Find each WBC.
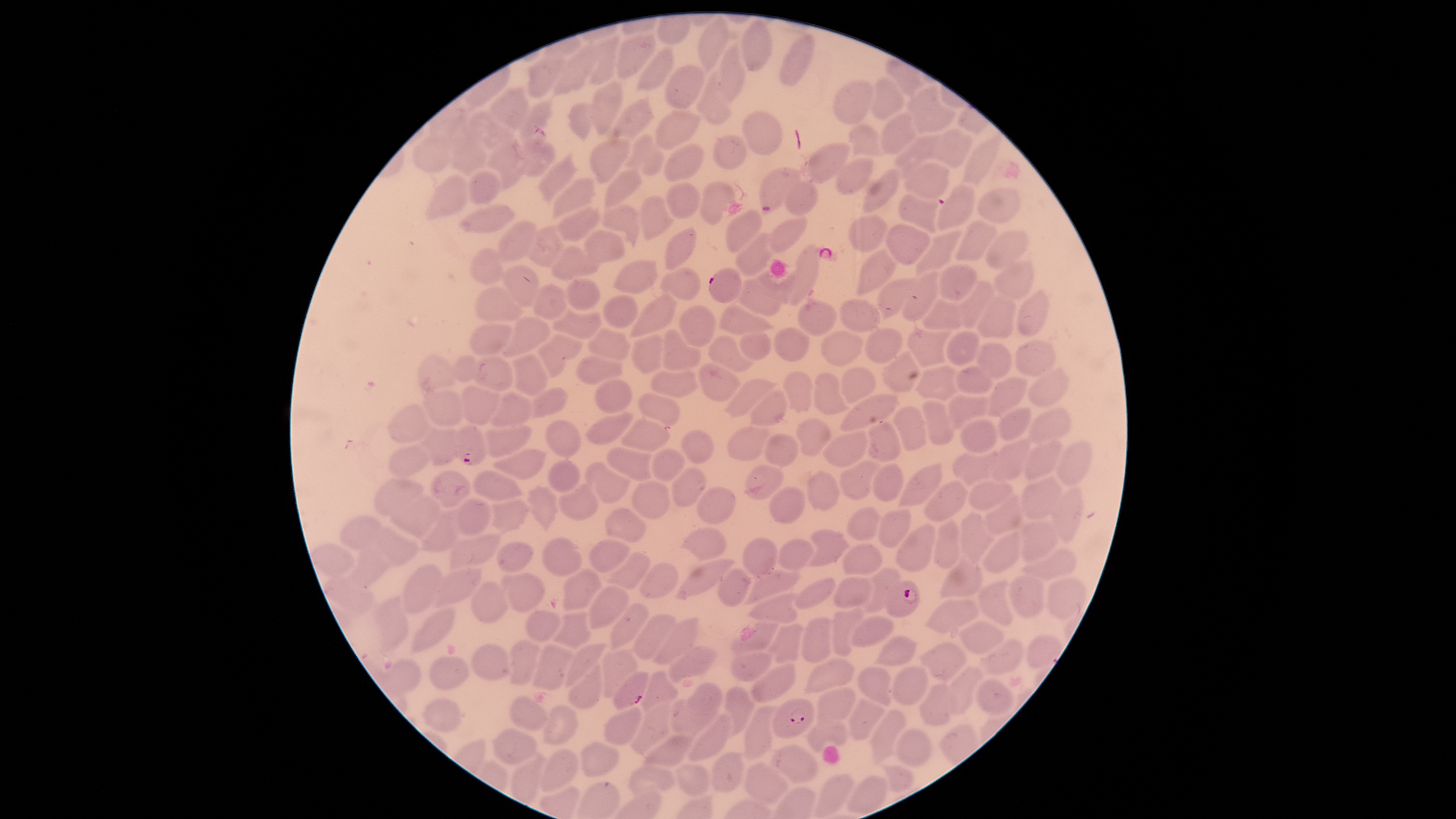
No WBCs identified.

Approximate bounding boxes, in pixels from the top-left corner.
Summary:
  - Parasitized RBCs: (left=520, top=124, right=555, bottom=177), (left=709, top=268, right=742, bottom=303), (left=453, top=425, right=489, bottom=466), (left=884, top=580, right=921, bottom=617), (left=611, top=672, right=650, bottom=710), (left=771, top=698, right=814, bottom=739)
  - Uninfected RBCs: (left=698, top=15, right=730, bottom=75), (left=740, top=19, right=772, bottom=75), (left=615, top=31, right=657, bottom=80), (left=778, top=32, right=815, bottom=86), (left=588, top=35, right=620, bottom=86), (left=717, top=37, right=747, bottom=105), (left=551, top=41, right=596, bottom=97), (left=636, top=46, right=674, bottom=93), (left=525, top=51, right=568, bottom=100), (left=664, top=64, right=707, bottom=109), (left=695, top=69, right=734, bottom=125), (left=871, top=77, right=904, bottom=120), (left=592, top=80, right=623, bottom=136), (left=833, top=80, right=874, bottom=125), (left=906, top=84, right=957, bottom=133), (left=489, top=86, right=529, bottom=130), (left=611, top=92, right=656, bottom=141), (left=517, top=98, right=553, bottom=142), (left=567, top=102, right=596, bottom=142), (left=465, top=108, right=509, bottom=151), (left=741, top=109, right=783, bottom=157), (left=655, top=110, right=702, bottom=151), (left=878, top=113, right=918, bottom=155), (left=847, top=123, right=884, bottom=161), (left=928, top=130, right=972, bottom=169), (left=450, top=132, right=488, bottom=179), (left=961, top=132, right=1002, bottom=186), (left=485, top=133, right=526, bottom=193), (left=620, top=133, right=665, bottom=177), (left=894, top=133, right=942, bottom=176), (left=711, top=134, right=749, bottom=172), (left=411, top=135, right=453, bottom=174), (left=589, top=138, right=631, bottom=185), (left=663, top=142, right=704, bottom=183), (left=806, top=142, right=851, bottom=184), (left=537, top=149, right=579, bottom=204), (left=833, top=155, right=874, bottom=195), (left=904, top=162, right=951, bottom=201), (left=759, top=166, right=805, bottom=216), (left=604, top=167, right=644, bottom=207), (left=862, top=168, right=900, bottom=213), (left=466, top=169, right=501, bottom=204), (left=424, top=173, right=470, bottom=220), (left=551, top=176, right=597, bottom=220), (left=784, top=178, right=819, bottom=216), (left=699, top=180, right=736, bottom=226), (left=665, top=181, right=700, bottom=219), (left=935, top=183, right=975, bottom=230), (left=977, top=187, right=1020, bottom=224), (left=897, top=193, right=939, bottom=234), (left=639, top=194, right=675, bottom=241), (left=456, top=201, right=517, bottom=236), (left=600, top=204, right=642, bottom=248), (left=558, top=205, right=601, bottom=243), (left=725, top=208, right=763, bottom=254), (left=848, top=214, right=888, bottom=252), (left=770, top=216, right=808, bottom=252), (left=955, top=218, right=999, bottom=261), (left=494, top=219, right=537, bottom=265), (left=886, top=224, right=931, bottom=265), (left=526, top=225, right=566, bottom=267), (left=664, top=226, right=697, bottom=271), (left=581, top=229, right=626, bottom=265), (left=914, top=229, right=962, bottom=277), (left=985, top=230, right=1030, bottom=270), (left=733, top=231, right=777, bottom=277), (left=787, top=242, right=821, bottom=308), (left=550, top=246, right=600, bottom=281), (left=470, top=247, right=504, bottom=286), (left=855, top=248, right=898, bottom=297), (left=992, top=257, right=1034, bottom=298), (left=612, top=259, right=659, bottom=295), (left=501, top=263, right=540, bottom=307), (left=938, top=263, right=978, bottom=302), (left=660, top=267, right=701, bottom=302), (left=730, top=269, right=793, bottom=317), (left=901, top=270, right=939, bottom=321), (left=565, top=277, right=601, bottom=312), (left=877, top=277, right=917, bottom=320), (left=955, top=279, right=994, bottom=329), (left=531, top=283, right=569, bottom=320), (left=474, top=286, right=524, bottom=323), (left=1016, top=287, right=1049, bottom=336), (left=601, top=294, right=639, bottom=330), (left=628, top=294, right=678, bottom=338), (left=975, top=294, right=1017, bottom=340), (left=922, top=296, right=961, bottom=332), (left=797, top=298, right=838, bottom=337), (left=839, top=298, right=881, bottom=333), (left=679, top=304, right=716, bottom=347), (left=717, top=304, right=775, bottom=335), (left=552, top=305, right=601, bottom=339), (left=501, top=316, right=551, bottom=359), (left=469, top=323, right=514, bottom=357), (left=906, top=326, right=953, bottom=368), (left=586, top=327, right=632, bottom=361), (left=773, top=327, right=810, bottom=362), (left=661, top=328, right=703, bottom=372), (left=864, top=328, right=904, bottom=364), (left=820, top=329, right=865, bottom=367), (left=945, top=329, right=981, bottom=367), (left=738, top=332, right=772, bottom=360), (left=536, top=333, right=585, bottom=382), (left=631, top=334, right=665, bottom=373), (left=707, top=335, right=756, bottom=373), (left=1015, top=339, right=1057, bottom=377), (left=976, top=342, right=1013, bottom=378), (left=882, top=349, right=921, bottom=392), (left=510, top=353, right=550, bottom=398), (left=418, top=354, right=455, bottom=392), (left=470, top=354, right=514, bottom=391), (left=452, top=355, right=479, bottom=384), (left=574, top=355, right=623, bottom=385), (left=697, top=360, right=742, bottom=401), (left=914, top=363, right=961, bottom=402), (left=954, top=365, right=991, bottom=395), (left=1025, top=365, right=1071, bottom=408), (left=840, top=367, right=876, bottom=403), (left=650, top=370, right=700, bottom=399), (left=782, top=370, right=814, bottom=414), (left=812, top=371, right=853, bottom=415), (left=721, top=377, right=782, bottom=418), (left=986, top=377, right=1029, bottom=417), (left=594, top=379, right=633, bottom=415), (left=460, top=385, right=502, bottom=425), (left=530, top=386, right=568, bottom=418), (left=422, top=388, right=464, bottom=428), (left=490, top=389, right=533, bottom=427), (left=749, top=389, right=790, bottom=427), (left=638, top=392, right=681, bottom=427), (left=840, top=392, right=898, bottom=431), (left=945, top=392, right=990, bottom=430), (left=922, top=398, right=955, bottom=445), (left=387, top=404, right=432, bottom=443), (left=893, top=405, right=928, bottom=453), (left=998, top=406, right=1032, bottom=442), (left=1028, top=406, right=1072, bottom=443), (left=585, top=410, right=633, bottom=445), (left=620, top=416, right=671, bottom=453), (left=545, top=417, right=583, bottom=458), (left=794, top=418, right=831, bottom=457), (left=960, top=418, right=998, bottom=454), (left=867, top=421, right=901, bottom=464), (left=484, top=424, right=533, bottom=459), (left=420, top=425, right=458, bottom=467), (left=726, top=425, right=771, bottom=462), (left=680, top=429, right=715, bottom=465), (left=822, top=429, right=869, bottom=468), (left=762, top=433, right=799, bottom=468), (left=991, top=436, right=1031, bottom=482), (left=1024, top=437, right=1064, bottom=480), (left=1056, top=439, right=1093, bottom=486), (left=387, top=443, right=430, bottom=481), (left=606, top=446, right=657, bottom=482), (left=491, top=447, right=547, bottom=480), (left=651, top=448, right=686, bottom=482), (left=951, top=449, right=999, bottom=486), (left=838, top=457, right=884, bottom=501), (left=546, top=458, right=581, bottom=493), (left=584, top=461, right=634, bottom=504), (left=897, top=461, right=943, bottom=507), (left=744, top=462, right=784, bottom=500), (left=871, top=462, right=902, bottom=501), (left=672, top=465, right=707, bottom=506), (left=429, top=469, right=473, bottom=510), (left=472, top=469, right=525, bottom=501), (left=806, top=469, right=841, bottom=511), (left=1021, top=474, right=1064, bottom=520), (left=373, top=476, right=424, bottom=516), (left=923, top=479, right=971, bottom=523), (left=968, top=479, right=1013, bottom=511), (left=631, top=480, right=671, bottom=520), (left=558, top=482, right=599, bottom=521), (left=526, top=484, right=560, bottom=534), (left=769, top=484, right=806, bottom=526), (left=1051, top=486, right=1084, bottom=545), (left=694, top=487, right=736, bottom=525), (left=981, top=493, right=1025, bottom=535), (left=389, top=496, right=441, bottom=539), (left=454, top=497, right=491, bottom=537), (left=490, top=498, right=531, bottom=534), (left=845, top=506, right=882, bottom=542), (left=604, top=507, right=648, bottom=544), (left=877, top=507, right=913, bottom=549), (left=417, top=509, right=460, bottom=551), (left=958, top=510, right=995, bottom=568), (left=338, top=515, right=383, bottom=551), (left=931, top=520, right=961, bottom=571), (left=1019, top=521, right=1057, bottom=562), (left=895, top=522, right=936, bottom=573), (left=372, top=526, right=420, bottom=567), (left=680, top=526, right=728, bottom=562), (left=805, top=528, right=851, bottom=568), (left=981, top=528, right=1021, bottom=573), (left=448, top=533, right=501, bottom=570), (left=541, top=535, right=583, bottom=577), (left=742, top=537, right=779, bottom=578), (left=778, top=537, right=815, bottom=569), (left=588, top=538, right=631, bottom=574), (left=496, top=540, right=533, bottom=575), (left=842, top=543, right=884, bottom=577), (left=349, top=547, right=389, bottom=586), (left=1022, top=547, right=1077, bottom=581), (left=605, top=551, right=651, bottom=589), (left=675, top=558, right=737, bottom=600), (left=939, top=558, right=984, bottom=599), (left=640, top=562, right=680, bottom=598), (left=402, top=563, right=443, bottom=616), (left=430, top=566, right=483, bottom=609), (left=716, top=566, right=754, bottom=608), (left=864, top=566, right=901, bottom=614), (left=563, top=567, right=603, bottom=612), (left=745, top=568, right=801, bottom=604), (left=500, top=571, right=545, bottom=613), (left=322, top=575, right=375, bottom=616), (left=833, top=576, right=875, bottom=609), (left=1007, top=576, right=1046, bottom=619), (left=793, top=577, right=837, bottom=609), (left=1046, top=577, right=1090, bottom=619), (left=977, top=579, right=1014, bottom=627), (left=471, top=580, right=509, bottom=623), (left=588, top=585, right=631, bottom=630), (left=748, top=589, right=799, bottom=624), (left=370, top=594, right=410, bottom=652), (left=925, top=599, right=980, bottom=633), (left=609, top=604, right=651, bottom=651), (left=410, top=606, right=457, bottom=655), (left=523, top=608, right=562, bottom=643), (left=830, top=609, right=866, bottom=656), (left=552, top=610, right=592, bottom=649), (left=632, top=612, right=677, bottom=660), (left=851, top=615, right=895, bottom=647), (left=801, top=616, right=836, bottom=665), (left=651, top=617, right=699, bottom=664), (left=728, top=620, right=782, bottom=656), (left=958, top=621, right=1005, bottom=655), (left=766, top=622, right=804, bottom=664), (left=873, top=634, right=921, bottom=668), (left=1025, top=634, right=1063, bottom=670), (left=507, top=638, right=541, bottom=686), (left=981, top=639, right=1025, bottom=676), (left=918, top=641, right=969, bottom=684), (left=471, top=642, right=509, bottom=681), (left=563, top=642, right=608, bottom=689), (left=529, top=644, right=574, bottom=690), (left=668, top=644, right=718, bottom=683), (left=600, top=648, right=641, bottom=697), (left=729, top=650, right=773, bottom=683), (left=428, top=654, right=470, bottom=691), (left=804, top=657, right=856, bottom=695), (left=386, top=659, right=421, bottom=695), (left=566, top=659, right=601, bottom=710), (left=750, top=663, right=797, bottom=704), (left=947, top=664, right=986, bottom=716), (left=891, top=665, right=930, bottom=706), (left=857, top=666, right=892, bottom=706), (left=641, top=669, right=679, bottom=714), (left=974, top=678, right=1015, bottom=715), (left=685, top=682, right=723, bottom=714), (left=917, top=683, right=959, bottom=727), (left=723, top=685, right=757, bottom=738), (left=817, top=685, right=857, bottom=721), (left=508, top=694, right=549, bottom=732), (left=421, top=697, right=462, bottom=733), (left=847, top=698, right=888, bottom=742), (left=669, top=699, right=719, bottom=739), (left=629, top=700, right=671, bottom=755), (left=540, top=703, right=580, bottom=744), (left=742, top=704, right=782, bottom=761), (left=604, top=706, right=643, bottom=746), (left=868, top=709, right=907, bottom=769), (left=686, top=713, right=731, bottom=762), (left=806, top=718, right=849, bottom=753), (left=488, top=727, right=539, bottom=763), (left=896, top=727, right=933, bottom=767), (left=641, top=733, right=694, bottom=769), (left=580, top=740, right=620, bottom=778), (left=770, top=743, right=817, bottom=784), (left=540, top=748, right=580, bottom=791), (left=509, top=750, right=547, bottom=805), (left=711, top=750, right=745, bottom=793), (left=743, top=761, right=789, bottom=805), (left=675, top=762, right=710, bottom=797), (left=879, top=762, right=915, bottom=792), (left=628, top=763, right=675, bottom=796), (left=814, top=773, right=854, bottom=818), (left=846, top=774, right=888, bottom=815)
  - Stain: Giemsa
  - Visible region: circular
  - Image size: 1456×819 pixels
  - Field of view: single
  - Presence: malaria parasites detected
  - Capture: smartphone photograph through the microscope eyepiece
  - Species: Plasmodium falciparum
  - Preparation: thin blood smear